Report the malaria status of this cell.
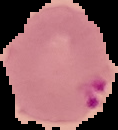

It is parasitized.

The area outside the segmented cell region is set to black. Image is 118×130 pixels. From a thin blood film.